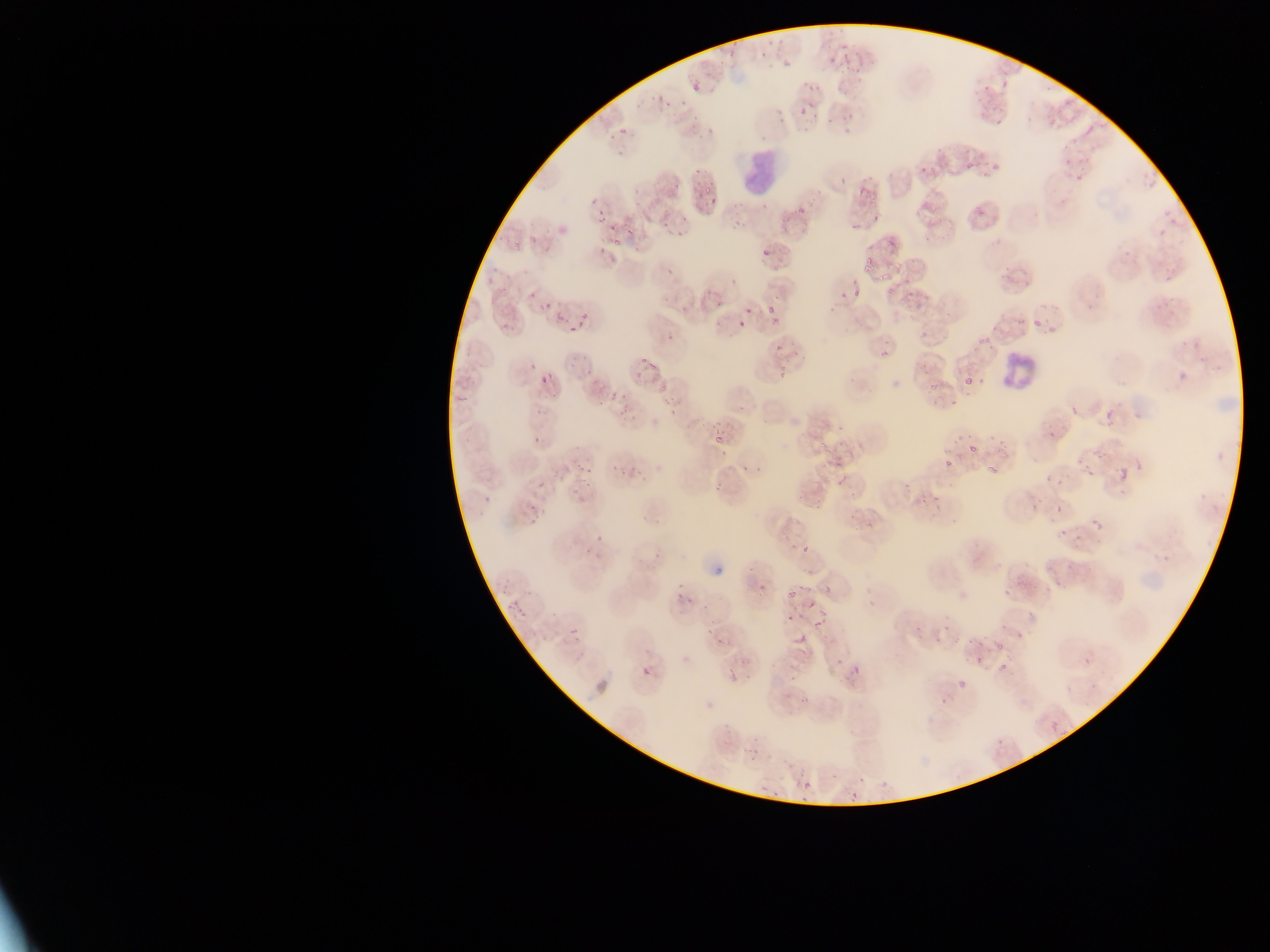
Approximate bounding boxes as {left, top, right, bottom} in pixels.
Summary:
  - Malaria parasite locations: {727, 51, 736, 59}, {782, 61, 790, 67}, {690, 81, 704, 96}, {1002, 82, 1010, 89}, {808, 84, 815, 92}, {666, 101, 672, 109}, {800, 105, 810, 117}, {849, 112, 855, 120}, {995, 117, 1005, 125}, {619, 127, 629, 138}, {610, 134, 616, 142}, {1060, 143, 1071, 149}, {1083, 156, 1093, 163}, {1063, 159, 1073, 167}, {965, 161, 973, 170}, {990, 163, 1003, 172}, {695, 167, 701, 175}, {930, 168, 938, 176}, {1075, 174, 1084, 181}, {840, 177, 848, 184}, {706, 187, 712, 195}, {710, 195, 720, 204}, {868, 201, 877, 209}, {597, 206, 608, 215}, {1157, 225, 1168, 239}, {607, 226, 617, 232}, {625, 227, 633, 235}, {532, 236, 538, 244}, {614, 238, 621, 247}, {887, 239, 895, 248}, {763, 247, 773, 257}, {597, 249, 606, 255}, {864, 258, 875, 269}, {853, 289, 862, 299}, {839, 292, 847, 300}, {528, 294, 536, 301}, {714, 301, 722, 307}, {545, 302, 553, 307}, {747, 305, 753, 315}, {767, 306, 775, 314}, {580, 311, 587, 320}, {556, 314, 564, 322}, {773, 316, 783, 324}, {1033, 317, 1043, 327}, {738, 318, 745, 326}, {500, 320, 515, 335}, {569, 325, 575, 333}, {878, 347, 892, 363}, {639, 358, 647, 364}, {530, 363, 536, 371}, {648, 364, 659, 372}, {583, 366, 594, 374}, {1171, 369, 1189, 390}, {777, 370, 785, 380}, {539, 373, 552, 387}, {963, 376, 977, 390}, {929, 383, 938, 390}, {609, 392, 617, 400}, {619, 407, 628, 416}, {1101, 408, 1119, 429}, {715, 420, 723, 425}, {1048, 428, 1060, 437}, {534, 435, 540, 443}, {714, 436, 725, 446}, {819, 440, 827, 449}, {968, 442, 981, 453}, {720, 447, 730, 456}, {1098, 449, 1109, 458}, {944, 458, 957, 471}, {742, 463, 753, 473}, {612, 464, 618, 472}, {987, 464, 998, 472}, {1115, 465, 1133, 486}, {1083, 467, 1097, 482}, {1054, 479, 1065, 485}, {537, 480, 548, 489}, {585, 482, 593, 487}, {713, 483, 721, 490}, {572, 490, 580, 495}, {482, 494, 495, 507}, {528, 502, 538, 513}, {1031, 502, 1039, 510}, {1090, 516, 1107, 535}, {527, 519, 535, 526}, {1059, 530, 1067, 536}, {800, 542, 812, 555}, {1055, 580, 1062, 588}, {760, 581, 768, 591}, {801, 584, 812, 593}, {501, 586, 509, 593}, {787, 591, 795, 599}, {677, 592, 683, 600}, {514, 599, 519, 610}, {809, 600, 819, 609}, {815, 607, 828, 615}, {517, 610, 525, 617}, {787, 614, 793, 622}, {812, 618, 823, 627}, {704, 623, 727, 644}, {569, 627, 581, 640}, {1016, 628, 1023, 641}, {996, 642, 1003, 650}, {723, 658, 744, 683}, {999, 661, 1009, 672}, {849, 663, 864, 681}, {642, 666, 653, 678}, {957, 680, 965, 690}, {1047, 719, 1063, 738}, {997, 739, 1005, 746}, {739, 740, 769, 761}, {802, 780, 813, 792}, {843, 788, 866, 800} | approximate {x, y} pixel centers of objects too small to bound: {734, 44}, {763, 55}, {845, 57}, {857, 72}, {986, 86}, {814, 116}, {829, 119}, {845, 119}, {924, 168}, {676, 185}, {861, 192}, {594, 200}, {801, 209}, {876, 216}, {684, 217}, {600, 220}, {665, 225}, {854, 227}, {679, 233}, {518, 242}, {635, 249}, {669, 270}, {881, 276}, {732, 282}, {891, 291}, {580, 325}, {669, 338}, {779, 348}, {583, 359}, {661, 389}, {623, 397}, {600, 404}, {1074, 410}, {1080, 462}, {581, 469}, {590, 470}, {623, 474}, {1050, 478}, {839, 481}, {1059, 509}, {599, 539}, {589, 548}, {750, 570}, {800, 588}, {690, 602}, {704, 606}, {509, 607}, {980, 644}, {978, 661}, {941, 702}
  - Leukocyte locations: {738, 145, 786, 199}, {998, 352, 1038, 389}
  - Country: Ghana
  - Image size: 1270×952 pixels
  - Capture: mobile-phone photograph through a microscope
  - Preparation: thin blood smear
  - Field of view: single